Identify the parasite.
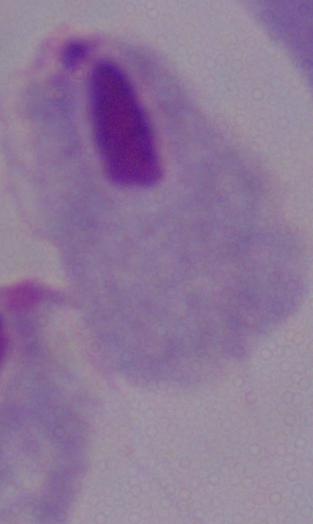
This is a trichomonad.

{
  "magnification": "1000x",
  "modality": "micrograph"
}